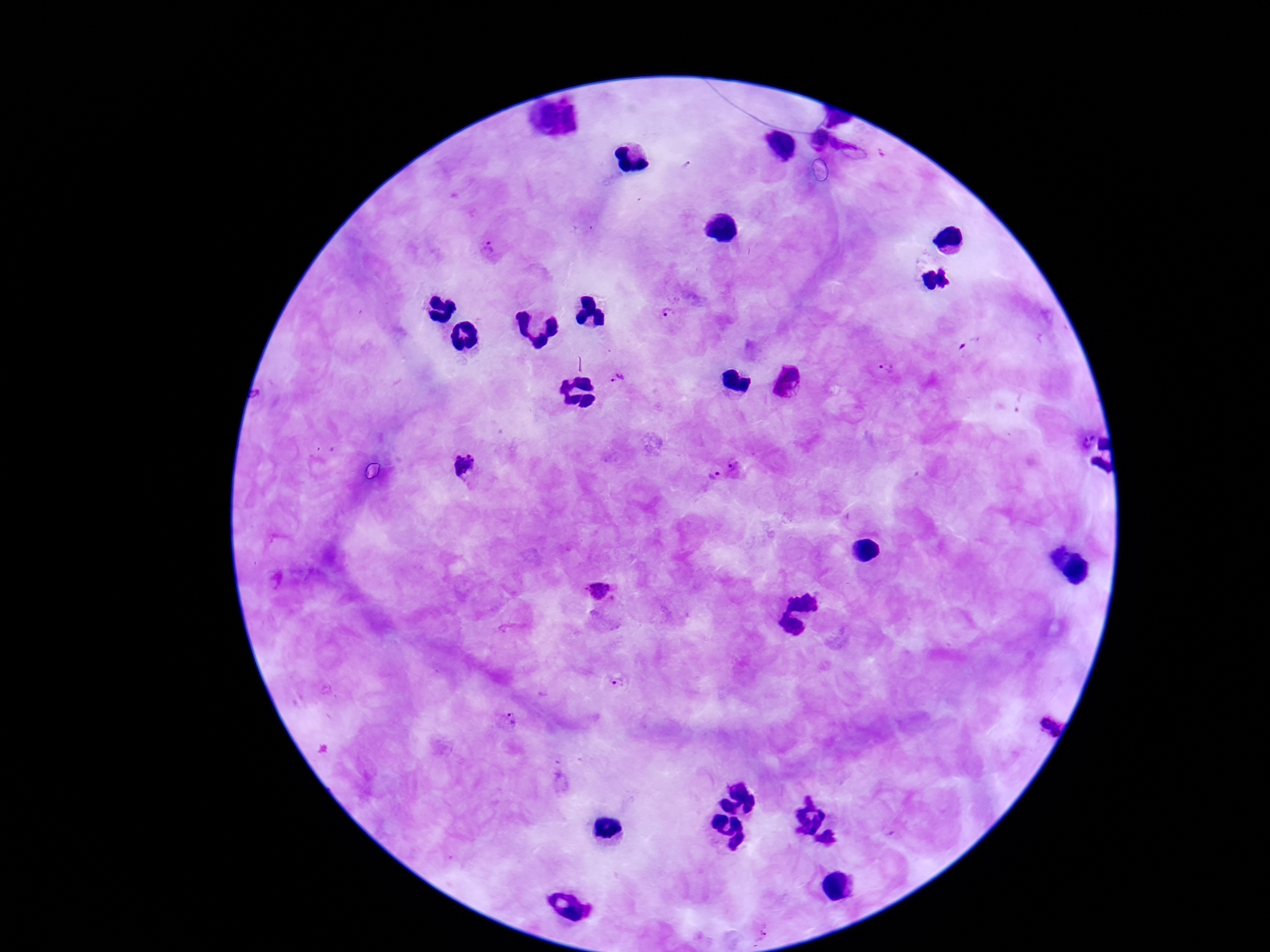 Approximate centers as [x, y] in pixels. Plasmodium parasite locations: [816, 139], [852, 146], [489, 251], [671, 315], [887, 370], [622, 377], [788, 381], [1086, 442], [737, 463], [459, 465], [713, 476], [598, 591], [617, 682], [510, 720], [1042, 720], [809, 797], [762, 932]. Single field of view. Giemsa stain. 100x magnification. Smartphone photograph taken through the microscope eyepiece. Thick blood film. Image is 1270×952 pixels. Patient malaria status: infected.